Assess this cell for malaria.
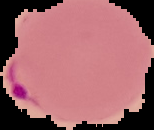
Parasitized.

The area outside the segmented cell region is set to black. From a thin blood film. Image is 154×130 pixels.